Locate and identify every blood parasite.
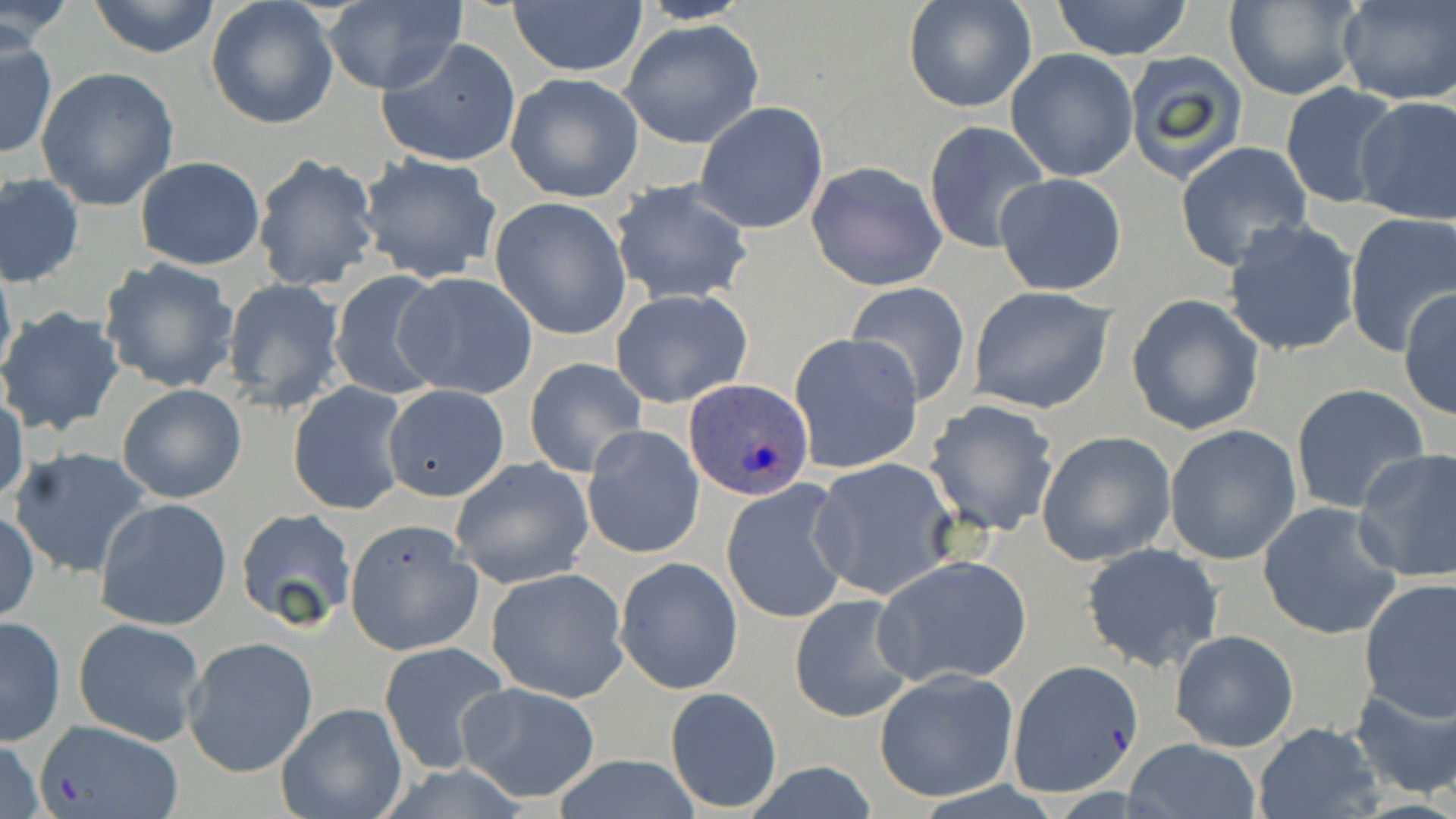
Approximate bounding boxes as (x1, y1, x2, y2) in pixels.
Plasmodium ovale-infected red blood cells: (683, 378, 813, 501).
No Plasmodium falciparum, Plasmodium malariae, Plasmodium vivax, Babesia divergens, or Trypanosoma brucei observed.

{
  "slide_level_diagnosis": "Plasmodium ovale",
  "field_of_view": "one of a larger specimen",
  "uninfected_red_blood_cell_locations": "approximate bounding boxes as (x1, y1, x2, y2) in pixels: (85, 0, 222, 58), (902, 0, 1037, 114), (1047, 0, 1196, 62), (1223, 0, 1362, 100), (0, 1, 72, 52), (206, 1, 340, 130), (507, 1, 647, 78), (634, 1, 758, 24), (1336, 1, 1455, 105), (318, 3, 465, 94), (621, 20, 764, 147), (0, 30, 56, 159), (376, 38, 522, 169), (1006, 49, 1139, 182), (1123, 53, 1250, 184), (35, 66, 181, 212), (505, 74, 642, 201), (1280, 82, 1406, 212), (1352, 95, 1456, 229), (695, 101, 829, 234), (922, 120, 1050, 253), (1174, 141, 1312, 271), (356, 152, 504, 285), (252, 154, 380, 293), (135, 157, 266, 270), (805, 162, 946, 291), (994, 172, 1127, 298), (1, 175, 84, 286), (609, 180, 751, 307), (490, 196, 631, 341), (1344, 214, 1456, 355), (1221, 217, 1362, 358), (0, 255, 17, 385), (99, 258, 242, 394), (328, 269, 450, 401), (395, 271, 539, 400), (219, 278, 345, 412), (845, 283, 971, 405), (967, 286, 1115, 414), (1398, 288, 1455, 419), (611, 289, 752, 408), (1126, 293, 1265, 435), (0, 307, 127, 436), (789, 333, 926, 474), (524, 358, 648, 478), (288, 381, 410, 516), (117, 382, 247, 503), (1290, 383, 1431, 513), (382, 384, 509, 500), (0, 390, 27, 509), (262, 394, 388, 586), (924, 399, 1060, 536), (1164, 424, 1302, 565), (581, 425, 704, 560), (1036, 431, 1177, 566), (8, 446, 158, 581), (1352, 447, 1456, 583), (809, 457, 958, 601), (449, 458, 594, 588), (720, 479, 855, 623), (94, 495, 234, 632), (1258, 502, 1404, 640), (235, 508, 357, 632), (1, 510, 40, 624), (343, 519, 482, 656), (1083, 543, 1223, 671), (873, 554, 1033, 686), (616, 558, 742, 694), (485, 567, 630, 703), (1357, 577, 1456, 722), (789, 595, 916, 721), (0, 615, 66, 745), (73, 617, 206, 744), (1168, 629, 1300, 752), (182, 636, 318, 778), (377, 640, 513, 775), (1010, 661, 1143, 797), (874, 668, 1018, 802), (1347, 676, 1456, 802), (456, 681, 601, 804), (665, 687, 782, 813), (276, 703, 407, 819), (30, 719, 186, 819), (1250, 722, 1385, 819), (0, 735, 46, 818), (1122, 739, 1261, 819), (548, 757, 706, 818), (736, 761, 884, 819)",
  "magnification": "1000x",
  "stain": "May-Grünwald-Giemsa",
  "preparation": "thin blood film",
  "image_size": "1456×819 pixels",
  "modality": "optical microscopy"
}